Name the parasite shown.
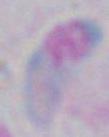

Toxoplasma gondii.

Summary:
  - Magnification: 1000x
  - Modality: photomicrograph